Outline each Plasmodium vivax-infected red blood cell.
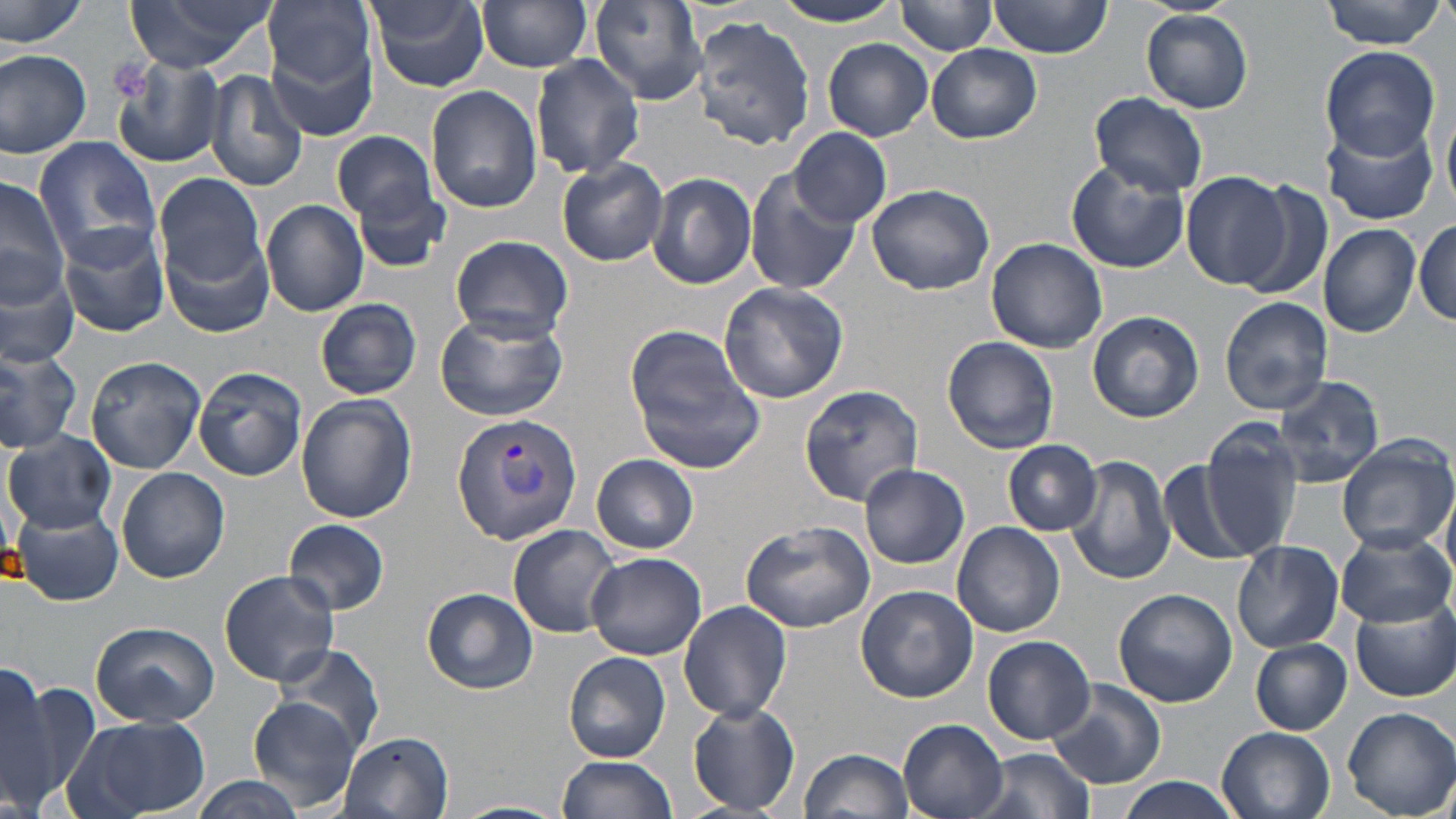

Approximate bounding boxes as [x1, y1, x2, y2] in pixels.
Plasmodium vivax-infected red blood cells: [451, 413, 583, 544].

Uninfected red blood cell locations: [1, 0, 90, 51], [127, 0, 274, 75], [264, 0, 375, 95], [589, 0, 706, 101], [988, 0, 1112, 58], [1319, 0, 1449, 49], [477, 1, 594, 73], [767, 1, 906, 26], [897, 1, 997, 57], [365, 2, 490, 91], [1141, 10, 1255, 112], [692, 17, 815, 149], [268, 34, 378, 143], [823, 38, 934, 141], [927, 44, 1042, 143], [1320, 45, 1442, 159], [0, 46, 93, 160], [0, 52, 198, 158], [112, 53, 224, 167], [530, 53, 646, 179], [206, 69, 309, 193], [425, 84, 543, 213], [1089, 92, 1208, 199], [1322, 116, 1439, 226], [790, 127, 891, 228], [333, 130, 438, 226], [32, 135, 164, 273], [558, 159, 667, 266], [1066, 161, 1189, 273], [744, 169, 861, 297], [1180, 170, 1289, 288], [647, 171, 757, 289], [154, 172, 265, 285], [0, 177, 72, 310], [1236, 177, 1336, 304], [353, 182, 451, 273], [867, 182, 994, 295], [261, 199, 369, 317], [56, 218, 172, 338], [1413, 219, 1455, 327], [1319, 224, 1421, 337], [161, 228, 275, 339], [449, 234, 573, 343], [985, 237, 1107, 353], [0, 261, 78, 367], [718, 282, 847, 404], [1220, 296, 1334, 414], [314, 298, 422, 399], [432, 309, 568, 422], [1087, 309, 1204, 423], [626, 327, 769, 472], [942, 336, 1060, 454], [0, 341, 83, 450], [85, 356, 205, 474], [192, 365, 307, 482], [1275, 376, 1384, 487], [799, 383, 924, 505], [296, 394, 416, 523], [1201, 422, 1306, 556], [4, 432, 117, 533], [1335, 437, 1454, 553], [1003, 440, 1102, 536], [591, 453, 698, 554], [1066, 454, 1174, 585], [1159, 460, 1258, 566], [859, 465, 970, 568], [116, 466, 230, 583], [12, 507, 123, 606], [284, 518, 390, 615], [742, 519, 878, 637], [952, 521, 1064, 638], [509, 524, 626, 638], [1335, 529, 1452, 626], [1232, 541, 1344, 653], [585, 551, 706, 660], [219, 571, 340, 685], [856, 584, 979, 702], [422, 587, 538, 694], [1113, 588, 1237, 709], [1352, 598, 1455, 702], [678, 600, 792, 721], [89, 621, 219, 727], [983, 635, 1095, 744], [1249, 639, 1352, 735], [269, 640, 388, 759], [1237, 641, 1348, 819], [565, 652, 672, 763], [0, 662, 59, 809], [8, 677, 104, 809], [1047, 677, 1167, 790], [247, 695, 365, 815], [687, 702, 801, 813], [1342, 706, 1456, 816], [67, 716, 208, 819], [898, 718, 1008, 819], [1216, 727, 1334, 819], [338, 730, 456, 819], [969, 747, 1096, 819], [800, 748, 914, 819], [556, 755, 677, 819], [189, 777, 301, 819], [1111, 777, 1244, 819], [454, 798, 568, 819]. Slide-level diagnosis: Plasmodium vivax. Single field of view. Optical microscopy. Image is 1456×819 pixels. 1000x magnification. Thin blood smear. May-Grünwald-Giemsa stain.